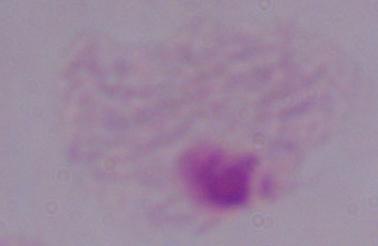
modality = photomicrograph
magnification = 1000x
identification = trichomonad